State which parasite is depicted.
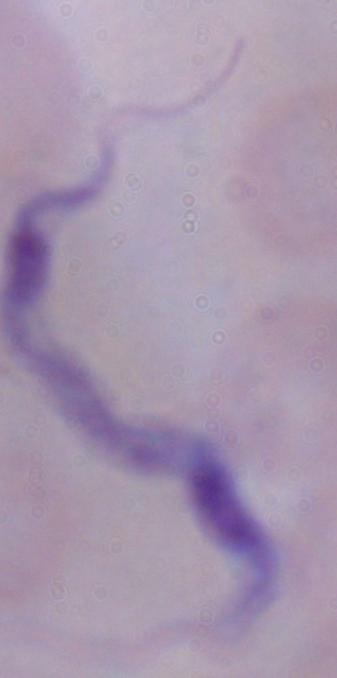

This is a trypanosome.

Micrograph. 1000x magnification.